Give the extent of all uninfected red blood cells.
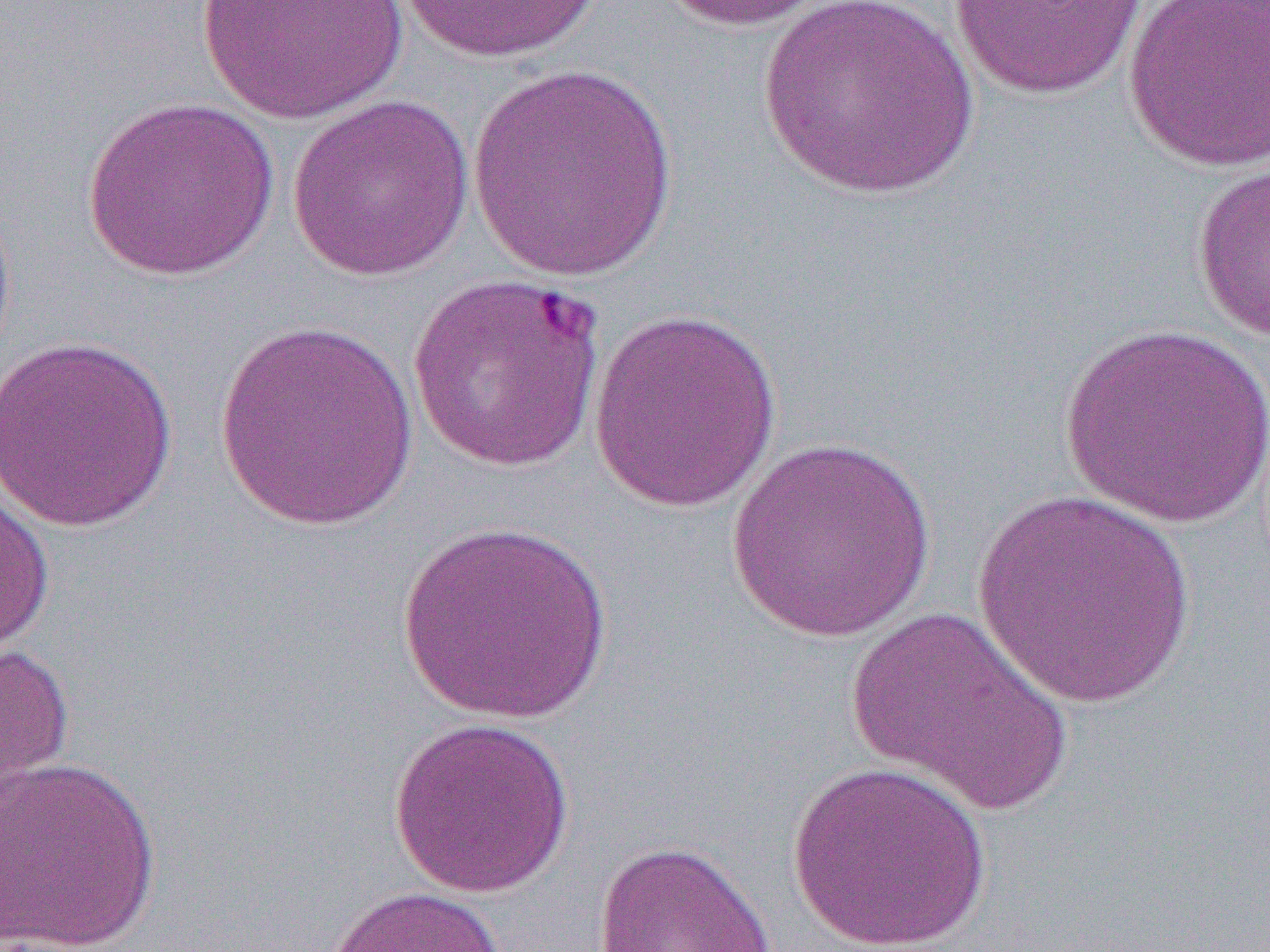

Approximate bounding boxes as named x1/y1/x2/y2 corners in pixels.
Uninfected red blood cells: (x1=195, y1=0, x2=410, y2=125), (x1=397, y1=0, x2=602, y2=65), (x1=653, y1=0, x2=838, y2=32), (x1=755, y1=0, x2=981, y2=200), (x1=950, y1=1, x2=1149, y2=101), (x1=1122, y1=1, x2=1270, y2=172), (x1=466, y1=64, x2=683, y2=283), (x1=285, y1=93, x2=476, y2=283), (x1=82, y1=96, x2=280, y2=282), (x1=1191, y1=162, x2=1270, y2=342), (x1=0, y1=192, x2=17, y2=374), (x1=405, y1=274, x2=608, y2=474), (x1=588, y1=307, x2=783, y2=513), (x1=214, y1=319, x2=420, y2=532), (x1=1057, y1=323, x2=1270, y2=528), (x1=0, y1=334, x2=179, y2=533), (x1=724, y1=436, x2=939, y2=643), (x1=0, y1=484, x2=55, y2=659), (x1=969, y1=489, x2=1200, y2=708), (x1=396, y1=522, x2=613, y2=724), (x1=846, y1=606, x2=1075, y2=817), (x1=0, y1=642, x2=75, y2=820), (x1=388, y1=716, x2=575, y2=899), (x1=0, y1=754, x2=163, y2=951), (x1=789, y1=761, x2=993, y2=951), (x1=591, y1=840, x2=777, y2=952), (x1=321, y1=884, x2=509, y2=952).

Slide-level diagnosis: Plasmodium falciparum. Single field of view. Image is 1270×952 pixels. Light microscopy. 1000x magnification. Thin blood film.